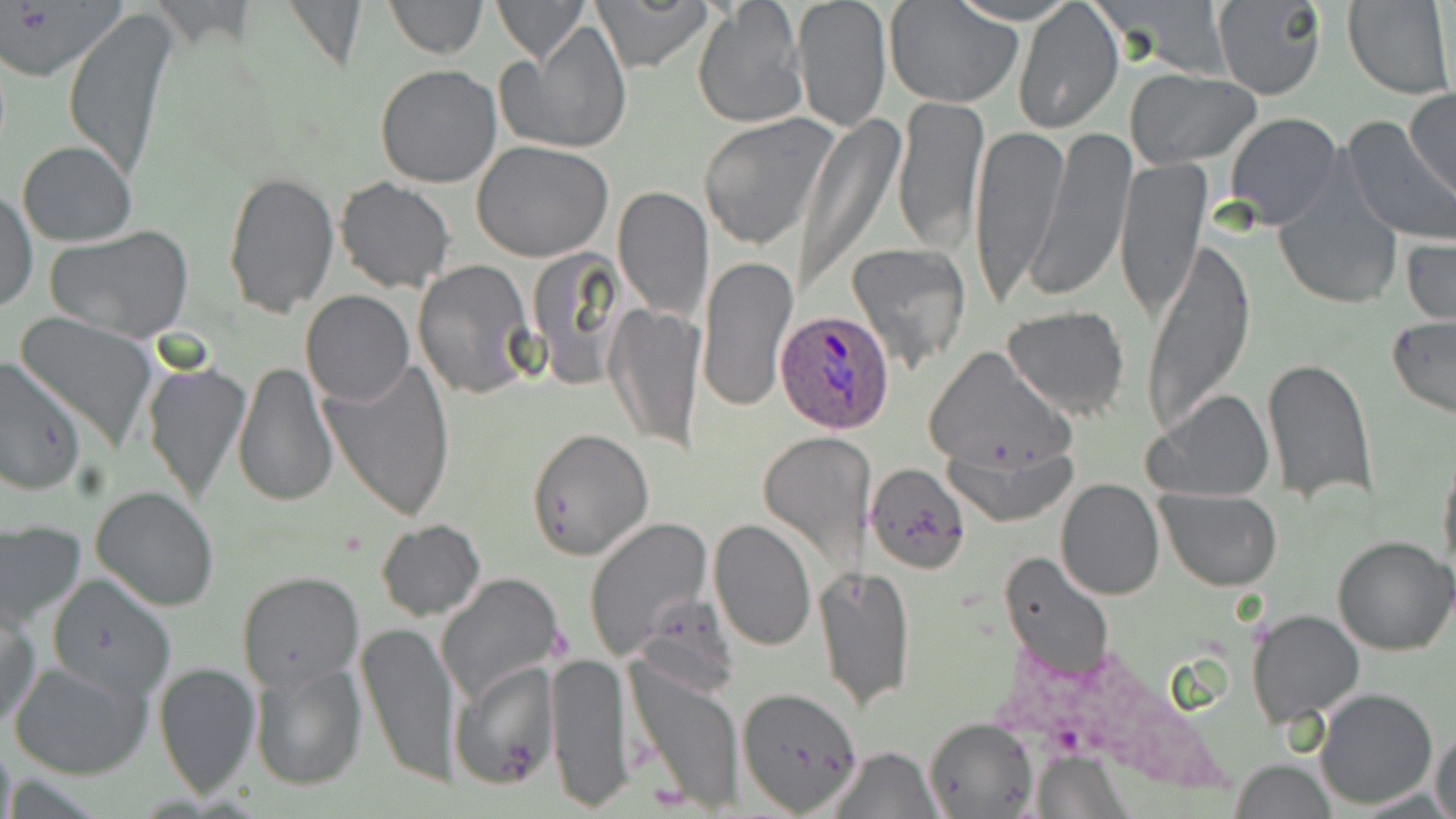
Summary:
  - Coordinate format: approximate bounding boxes as named x1/y1/x2/y2 corners in pixels
  - Uninfected red blood cell locations: (x1=279, y1=0, x2=369, y2=74), (x1=383, y1=0, x2=486, y2=58), (x1=493, y1=0, x2=590, y2=64), (x1=592, y1=0, x2=711, y2=72), (x1=792, y1=0, x2=892, y2=133), (x1=1091, y1=0, x2=1231, y2=79), (x1=1213, y1=0, x2=1327, y2=99), (x1=1341, y1=0, x2=1453, y2=98), (x1=1010, y1=1, x2=1123, y2=134), (x1=885, y1=2, x2=1024, y2=108), (x1=692, y1=3, x2=807, y2=130), (x1=63, y1=8, x2=178, y2=180), (x1=500, y1=20, x2=631, y2=155), (x1=374, y1=63, x2=503, y2=188), (x1=1125, y1=70, x2=1261, y2=168), (x1=1405, y1=88, x2=1455, y2=202), (x1=892, y1=96, x2=989, y2=254), (x1=1224, y1=111, x2=1343, y2=229), (x1=698, y1=113, x2=841, y2=251), (x1=796, y1=114, x2=900, y2=292), (x1=1340, y1=117, x2=1456, y2=246), (x1=969, y1=123, x2=1065, y2=306), (x1=1028, y1=127, x2=1136, y2=303), (x1=17, y1=140, x2=138, y2=246), (x1=472, y1=141, x2=615, y2=262), (x1=1115, y1=156, x2=1209, y2=324), (x1=221, y1=170, x2=341, y2=316), (x1=1273, y1=172, x2=1404, y2=311), (x1=334, y1=177, x2=456, y2=294), (x1=614, y1=186, x2=712, y2=322), (x1=1, y1=187, x2=37, y2=314), (x1=46, y1=224, x2=193, y2=344), (x1=1403, y1=230, x2=1455, y2=331), (x1=1140, y1=236, x2=1256, y2=437), (x1=845, y1=242, x2=969, y2=373), (x1=697, y1=255, x2=796, y2=413), (x1=414, y1=259, x2=537, y2=401), (x1=301, y1=291, x2=414, y2=406), (x1=606, y1=303, x2=704, y2=453), (x1=1001, y1=307, x2=1131, y2=421), (x1=14, y1=313, x2=161, y2=450), (x1=1386, y1=317, x2=1456, y2=419), (x1=923, y1=348, x2=1073, y2=475), (x1=0, y1=356, x2=85, y2=496), (x1=321, y1=357, x2=458, y2=522), (x1=1260, y1=359, x2=1378, y2=505), (x1=233, y1=360, x2=339, y2=508), (x1=143, y1=361, x2=250, y2=506), (x1=1143, y1=388, x2=1275, y2=503), (x1=526, y1=428, x2=653, y2=559), (x1=757, y1=431, x2=873, y2=573), (x1=943, y1=433, x2=1080, y2=528), (x1=1437, y1=446, x2=1456, y2=581), (x1=864, y1=462, x2=969, y2=576), (x1=1055, y1=478, x2=1165, y2=601), (x1=91, y1=486, x2=220, y2=611), (x1=1157, y1=488, x2=1283, y2=592), (x1=708, y1=517, x2=816, y2=651), (x1=375, y1=519, x2=486, y2=621), (x1=583, y1=519, x2=713, y2=661), (x1=1, y1=523, x2=87, y2=631), (x1=1332, y1=536, x2=1456, y2=656), (x1=1000, y1=551, x2=1114, y2=682), (x1=817, y1=565, x2=916, y2=711), (x1=236, y1=570, x2=365, y2=693), (x1=44, y1=574, x2=177, y2=703), (x1=437, y1=574, x2=561, y2=704), (x1=1, y1=601, x2=41, y2=731), (x1=1245, y1=610, x2=1364, y2=726), (x1=355, y1=618, x2=459, y2=788), (x1=547, y1=650, x2=634, y2=811), (x1=625, y1=657, x2=746, y2=812), (x1=9, y1=659, x2=152, y2=780), (x1=154, y1=659, x2=260, y2=797), (x1=248, y1=659, x2=366, y2=791), (x1=448, y1=660, x2=558, y2=789), (x1=736, y1=684, x2=864, y2=813), (x1=1315, y1=689, x2=1437, y2=809), (x1=922, y1=717, x2=1037, y2=819), (x1=1429, y1=726, x2=1455, y2=819), (x1=829, y1=745, x2=939, y2=818), (x1=1029, y1=752, x2=1129, y2=815), (x1=1230, y1=760, x2=1339, y2=817)
  - Plasmodium ovale-infected red blood cell locations: (x1=777, y1=307, x2=899, y2=434)
  - Slide-level diagnosis: Plasmodium ovale
  - Preparation: thin blood smear
  - Modality: optical microscopy
  - Image size: 1456×819 pixels
  - Field of view: single
  - Stain: May-Grünwald-Giemsa
  - Magnification: 1000x